Assess this cell for malaria.
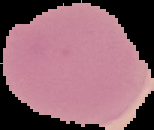

Uninfected.

Summary:
  - Image size: 154×130 pixels
  - Image type: segmented cell region on a black background
  - Preparation: thin blood smear